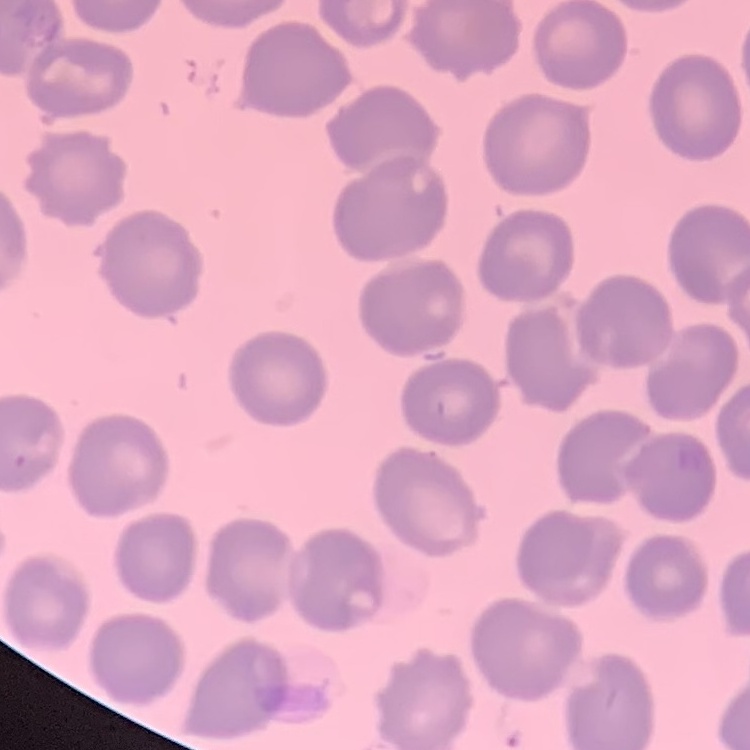
Summary:
  - Red blood cell morphology: no rouleaux formation
  - Image type: one tile cut from a larger photomicrograph
  - Preparation: thin blood film
  - Stain: Field's or Giemsa